State the blood parasite species.
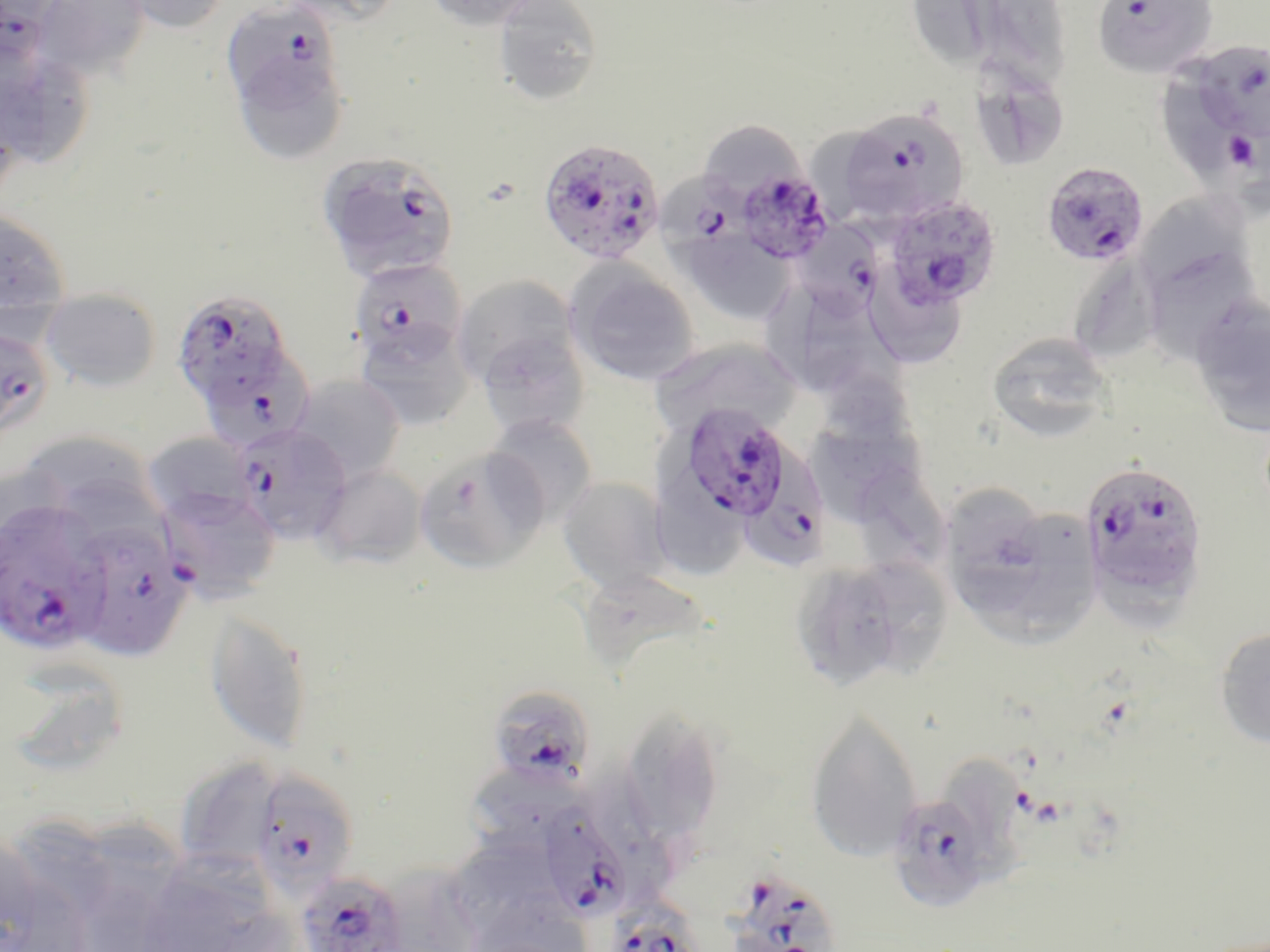
Plasmodium falciparum.

Approximate bounding boxes as (x1,y1)-(x2,y2) corner pairs in pixels. Uninfected red blood cell locations: (32,0)-(151,80), (115,0)-(232,34), (281,0)-(406,26), (424,0)-(544,31), (911,0)-(1006,71), (984,0)-(1078,90), (492,1)-(604,105), (227,42)-(353,169), (0,52)-(101,164), (1161,56)-(1258,185), (968,60)-(1070,171), (702,122)-(807,209), (805,126)-(916,212), (1145,192)-(1256,278), (336,198)-(455,287), (0,209)-(70,318), (677,227)-(796,324), (1141,244)-(1261,364), (1071,254)-(1178,357), (565,260)-(700,386), (871,263)-(963,366), (452,275)-(578,389), (40,288)-(161,392), (801,293)-(909,395), (1188,294)-(1270,436), (355,321)-(475,429), (476,326)-(588,439), (986,332)-(1114,441), (648,338)-(801,445), (289,374)-(406,484), (821,375)-(921,525), (484,413)-(597,527), (141,431)-(256,525), (30,438)-(144,522), (414,446)-(547,574), (863,463)-(948,573), (314,464)-(425,569), (655,471)-(750,582), (557,476)-(672,594), (948,481)-(1047,615), (979,506)-(1102,649), (788,557)-(938,692), (583,573)-(719,670), (204,610)-(314,755), (1214,625)-(1270,748), (16,662)-(122,775), (619,706)-(726,850), (804,707)-(923,864), (173,755)-(284,874), (949,755)-(1031,888), (459,766)-(585,851), (78,813)-(182,908), (0,838)-(92,952), (448,840)-(550,939), (151,849)-(272,952), (383,860)-(479,952). Platelet locations: (1227,132)-(1257,170). Plasmodium falciparum-infected red blood cell locations: (0,0)-(57,70), (219,0)-(345,119), (1091,0)-(1218,79), (1197,41)-(1270,137), (832,108)-(971,226), (538,138)-(665,264), (324,156)-(448,245), (1040,160)-(1149,267), (656,165)-(751,263), (736,167)-(833,263), (882,195)-(1002,313), (803,221)-(884,321), (348,257)-(468,368), (169,290)-(291,408), (0,335)-(55,438), (206,351)-(319,451), (677,400)-(794,524), (229,422)-(351,545), (744,439)-(831,568), (1080,460)-(1209,606), (154,484)-(282,603), (1,499)-(108,654), (70,522)-(192,660), (495,685)-(591,786), (251,770)-(359,895), (886,790)-(999,912), (537,801)-(634,923), (295,870)-(410,952), (732,870)-(847,952), (614,886)-(707,952). One field of a larger specimen. 1000x magnification. Light microscopy. May-Grünwald-Giemsa stain. Image is 1270×952 pixels. Thin blood film.